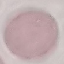
malaria status = uninfected
capture = smartphone through the microscope eyepiece
stain = Giemsa
preparation = thin smear
image type = automatically extracted cell patch, resized to 64 × 64 pixels